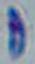
Summary:
  - Modality: photomicrograph
  - Magnification: 1000x
  - Identification: Toxoplasma gondii